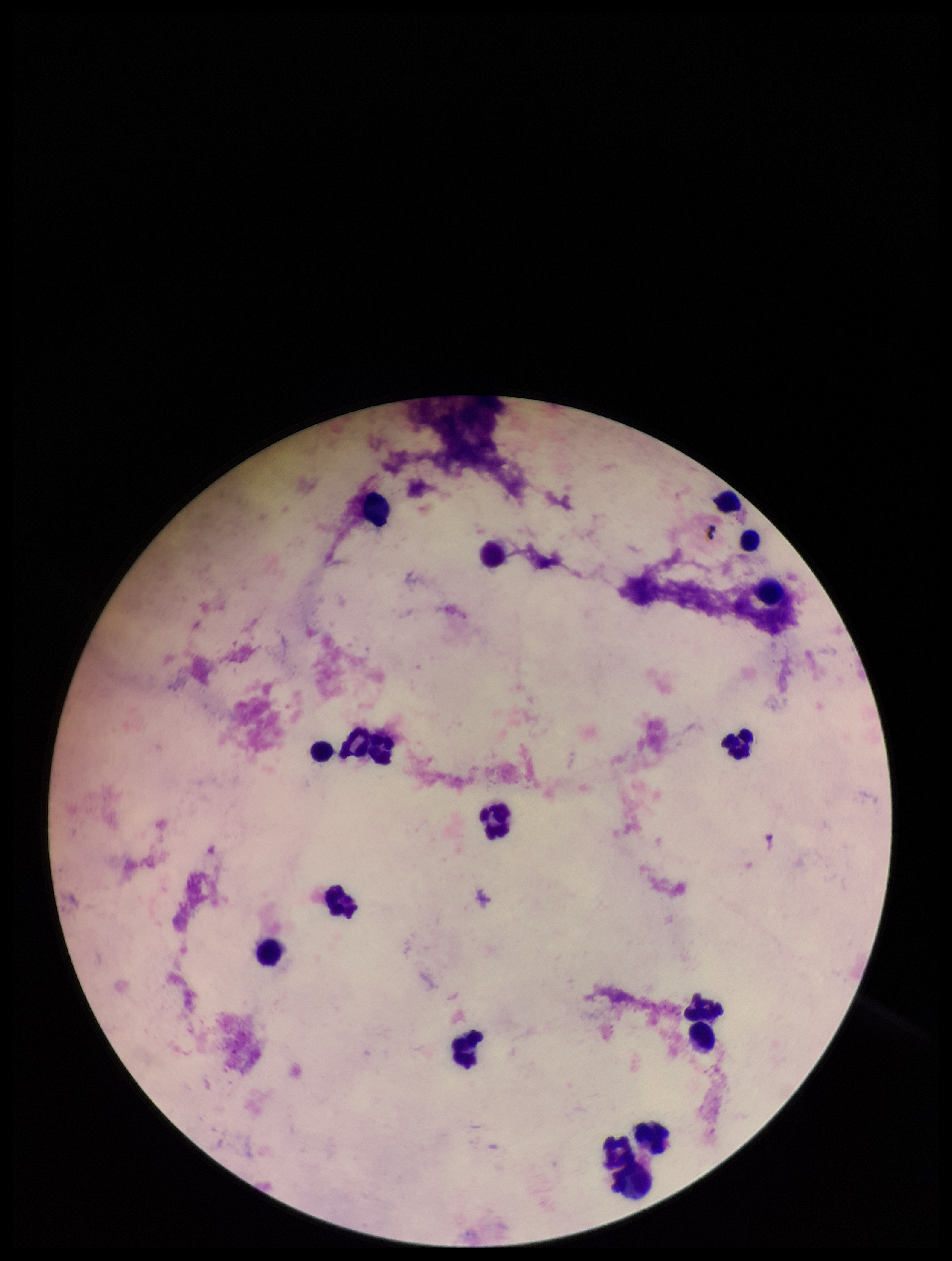

Summary:
  - Plasmodium parasites: none identified
  - Image size: 952×1261 pixels
  - Leukocyte count: 17
  - Field of view: one from this slide
  - Parasite count: 0
  - Capture: smartphone photograph through the microscope eyepiece
  - Stain: Giemsa
  - Preparation: thick
  - Patient malaria status: negative